Classify this cell by malaria status.
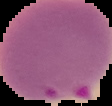
Parasitized.

From a thin blood smear. Image is 112×106 pixels. The area outside the segmented cell region is set to black.